Mark where leukocytes are.
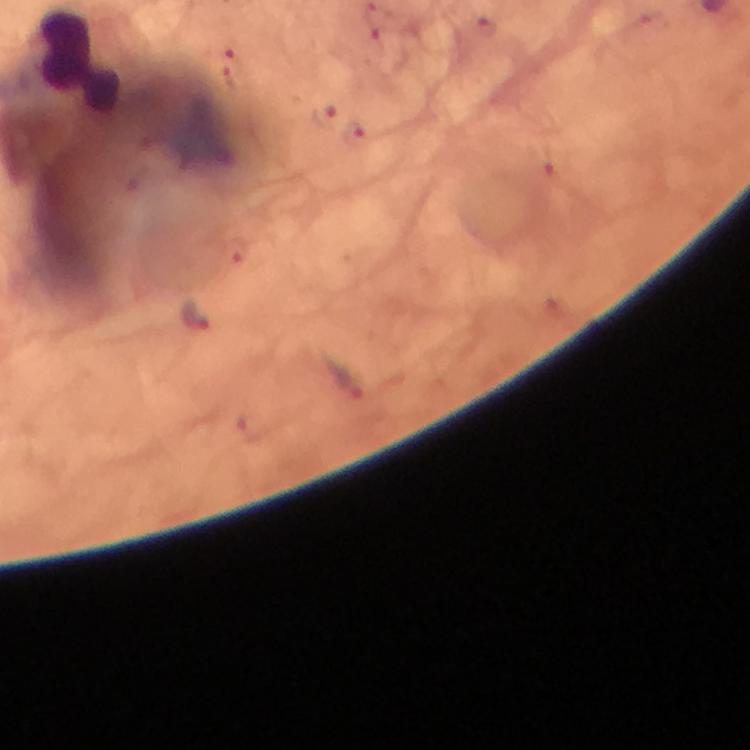
Approximate centers as [x, y] in pixels.
Leukocytes: [79, 62].

{
  "context": "from a malaria diagnostic workup",
  "stain": "Giemsa",
  "immersion_oil": "used",
  "cropped_from": "one field of view",
  "preparation": "thick blood smear",
  "image_size": "750×750 pixels",
  "malaria_parasite_locations": "approximate centers as [x, y] in pixels: [194, 315]",
  "capture": "smartphone mounted on the microscope",
  "magnification": "100x"
}